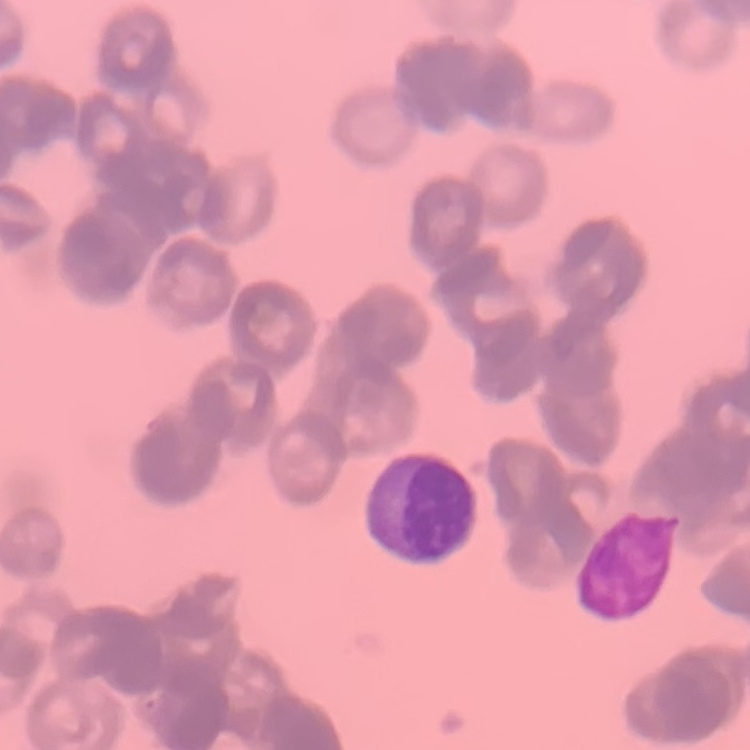
erythrocyte morphology = rouleaux formation
stain = Field's or Giemsa
image type = square crop of a larger photomicrograph
preparation = thin blood film